Identify the parasite.
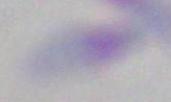

Toxoplasma gondii.

{
  "modality": "micrograph",
  "magnification": "1000x"
}